Locate platelets.
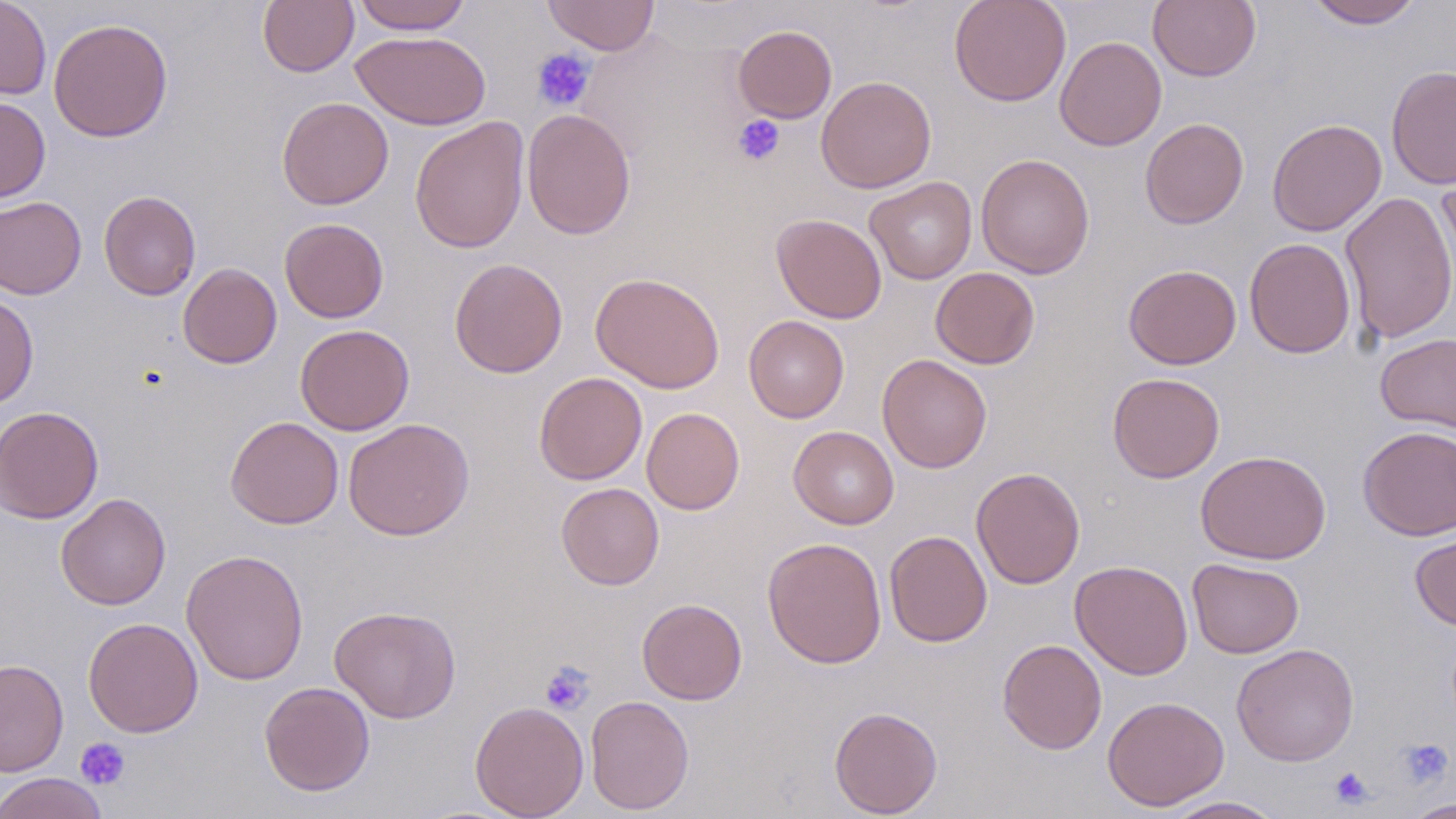
Approximate bounding boxes as (x1,y1)-(x2,y2) corner pairs in pixels.
Platelets: (532,48)-(596,112), (733,114)-(785,166), (539,660)-(595,715), (75,737)-(131,790), (1398,739)-(1453,788), (1329,766)-(1374,809).

Uninfected red blood cell locations: (0,0)-(51,100), (258,0)-(359,76), (351,0)-(473,34), (542,0)-(659,56), (949,0)-(1072,107), (1148,0)-(1261,82), (1306,0)-(1424,29), (48,18)-(174,143), (733,25)-(837,123), (351,30)-(490,130), (1054,35)-(1167,151), (1386,65)-(1456,190), (816,76)-(937,193), (0,96)-(51,203), (277,97)-(394,210), (521,108)-(636,240), (409,116)-(530,254), (1140,117)-(1249,228), (1267,118)-(1387,236), (976,153)-(1094,279), (1437,170)-(1456,304), (864,176)-(978,284), (98,190)-(201,300), (1338,191)-(1456,344), (0,196)-(86,299), (771,213)-(887,324), (279,217)-(389,323), (1244,238)-(1356,358), (449,258)-(568,378), (178,262)-(282,368), (1123,264)-(1242,369), (931,267)-(1040,369), (590,272)-(725,393), (0,292)-(39,409), (744,315)-(850,423), (295,324)-(414,436), (1375,333)-(1456,434), (877,354)-(992,473), (534,372)-(647,485), (1107,372)-(1225,482), (0,406)-(104,524), (641,407)-(745,514), (225,416)-(344,529), (343,418)-(475,541), (789,425)-(899,529), (1357,426)-(1456,540), (1195,449)-(1331,564), (970,467)-(1085,589), (556,482)-(664,590), (56,493)-(171,610), (1410,526)-(1456,631), (884,530)-(992,647), (762,536)-(887,669), (181,549)-(309,685), (1187,558)-(1304,659), (1070,560)-(1194,679), (637,598)-(747,705), (329,605)-(461,723), (82,617)-(203,737), (997,638)-(1107,755), (1231,643)-(1359,766), (0,659)-(69,777), (259,680)-(375,796), (585,695)-(694,815), (1102,696)-(1229,811), (469,700)-(589,819), (829,706)-(943,818), (0,772)-(109,819), (1161,796)-(1287,818), (1403,798)-(1455,818). Slide-level diagnosis: negative for blood parasites. May-Grünwald-Giemsa-stained preparation. Thin blood film. Image is 1456×819 pixels. 1000x magnification. One field of a larger specimen. Optical microscopy.